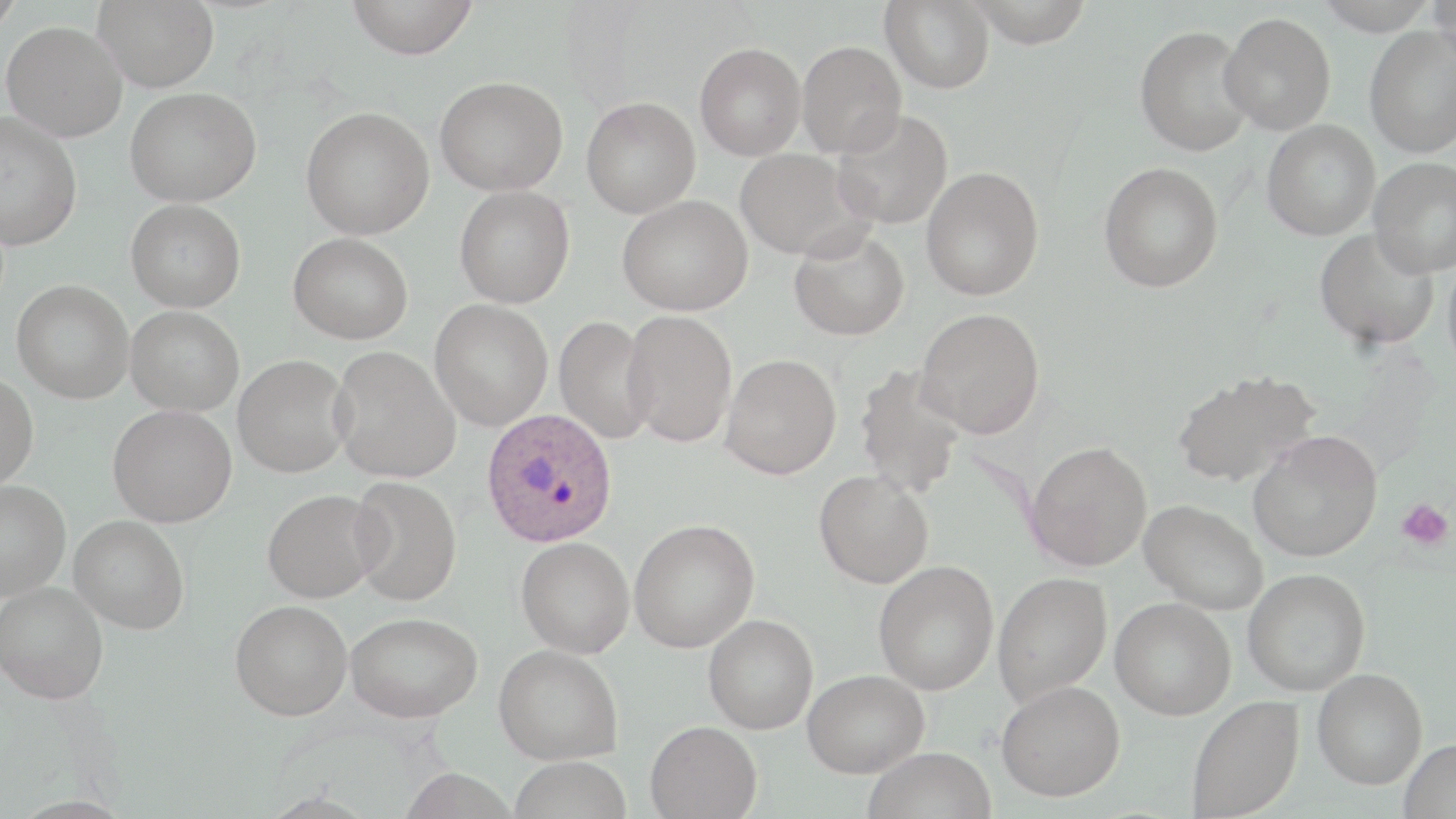

Summary:
  - Coordinate format: approximate bounding boxes as (x1,y1)-(x2,y2) corner pairs in pixels
  - Uninfected red blood cell locations: (0,0)-(24,38), (92,0)-(220,92), (345,0)-(479,59), (881,0)-(995,93), (964,0)-(1094,47), (1314,0)-(1440,35), (1429,0)-(1456,70), (1220,12)-(1336,135), (1,21)-(128,142), (1135,25)-(1255,156), (1364,25)-(1456,158), (797,40)-(906,157), (695,43)-(806,160), (435,76)-(568,196), (125,87)-(262,206), (581,97)-(701,218), (301,106)-(434,239), (832,107)-(953,230), (0,111)-(82,250), (1262,120)-(1381,240), (735,148)-(869,261), (1367,156)-(1456,277), (1098,162)-(1223,293), (921,166)-(1044,300), (455,186)-(575,308), (617,195)-(753,316), (126,198)-(246,312), (1314,226)-(1440,351), (788,227)-(910,341), (289,232)-(413,344), (1443,252)-(1456,380), (11,280)-(134,404), (430,299)-(553,431), (126,305)-(244,416), (915,308)-(1045,438), (622,310)-(737,446), (554,316)-(656,444), (329,346)-(461,483), (721,353)-(841,478), (232,355)-(352,477), (854,365)-(967,499), (1172,369)-(1321,488), (0,372)-(39,489), (108,405)-(237,527), (1248,430)-(1382,561), (1026,441)-(1152,571), (814,470)-(934,588), (348,476)-(462,606), (0,480)-(71,601), (262,488)-(386,603), (1140,500)-(1268,615), (69,515)-(189,634), (629,519)-(760,653), (516,536)-(635,658), (874,561)-(999,695), (1243,568)-(1370,696), (992,571)-(1112,707), (0,581)-(108,704), (1111,597)-(1236,719), (230,599)-(352,720), (345,612)-(483,722), (703,614)-(818,734), (494,644)-(623,764), (1312,668)-(1428,789), (802,669)-(929,778), (996,680)-(1125,801), (1187,695)-(1304,819), (645,720)-(762,819), (1399,738)-(1455,819), (862,746)-(997,819), (508,756)-(632,819)
  - Plasmodium ovale-infected red blood cell locations: (481,408)-(618,547)
  - Platelet locations: (1396,499)-(1453,551)
  - Slide-level diagnosis: Plasmodium ovale
  - Modality: light microscopy
  - Image size: 1456×819 pixels
  - Preparation: thin blood film
  - Stain: May-Grünwald-Giemsa
  - Magnification: 1000x
  - Field of view: single